Identify the cell.
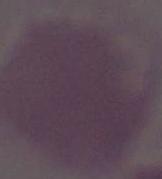

This is an erythrocyte.

{
  "modality": "photomicrograph",
  "magnification": "1000x"
}